State which cell type is depicted.
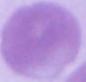

This is an erythrocyte.

Captured at 1000x magnification. Micrograph.